Comment on the morphology of the red blood cells.
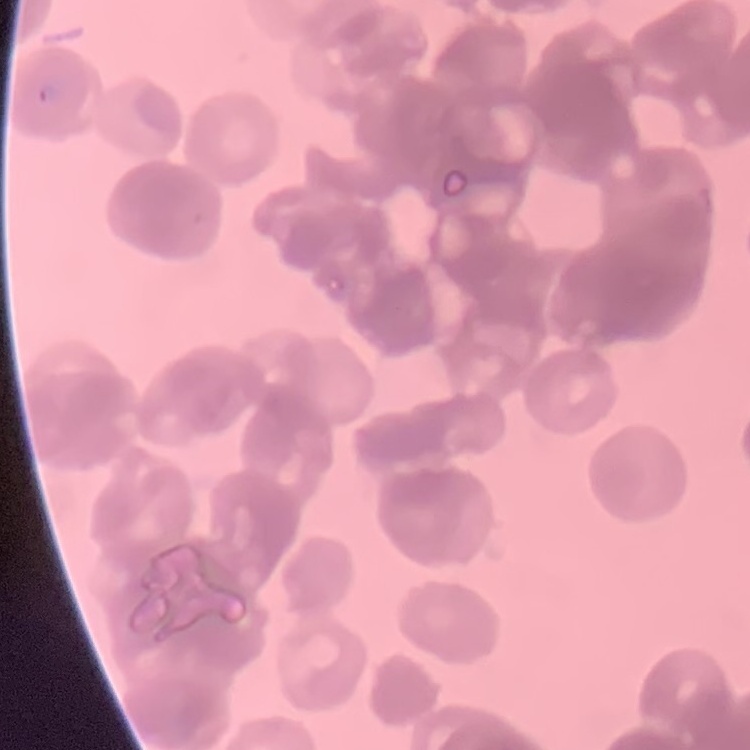
Rouleaux formation.

Summary:
  - Image type: one tile cut from a larger photomicrograph
  - Preparation: thin blood smear
  - Stain: Field's or Giemsa